Assess the morphology of the erythrocytes.
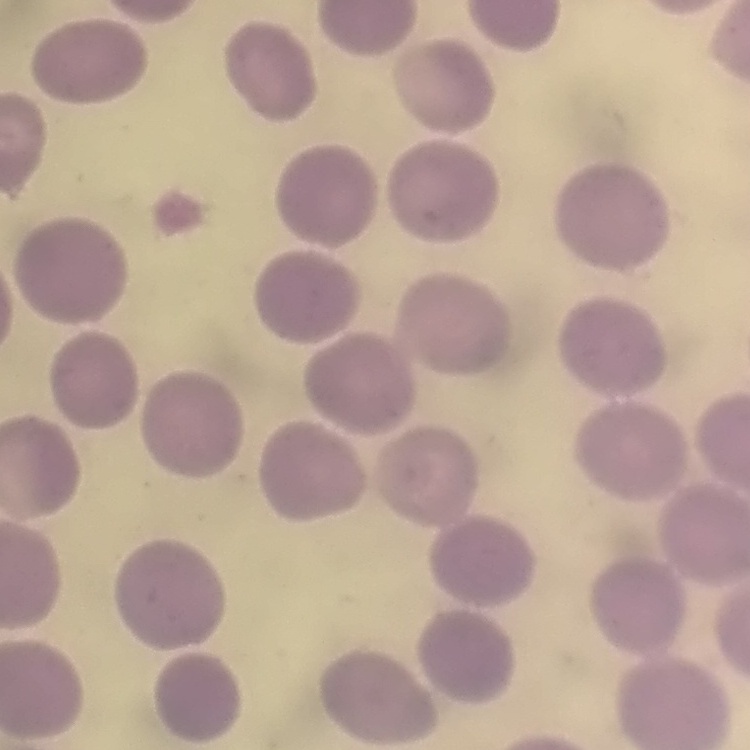

They show no rouleaux formation.

Summary:
  - Image type: square crop of a larger photomicrograph
  - Preparation: thin blood smear
  - Stain: Field's or Giemsa